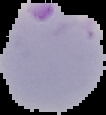

From a thin blood film. Result: malaria parasites identified. Image is 106×115 pixels. The area outside the segmented cell region is set to black.